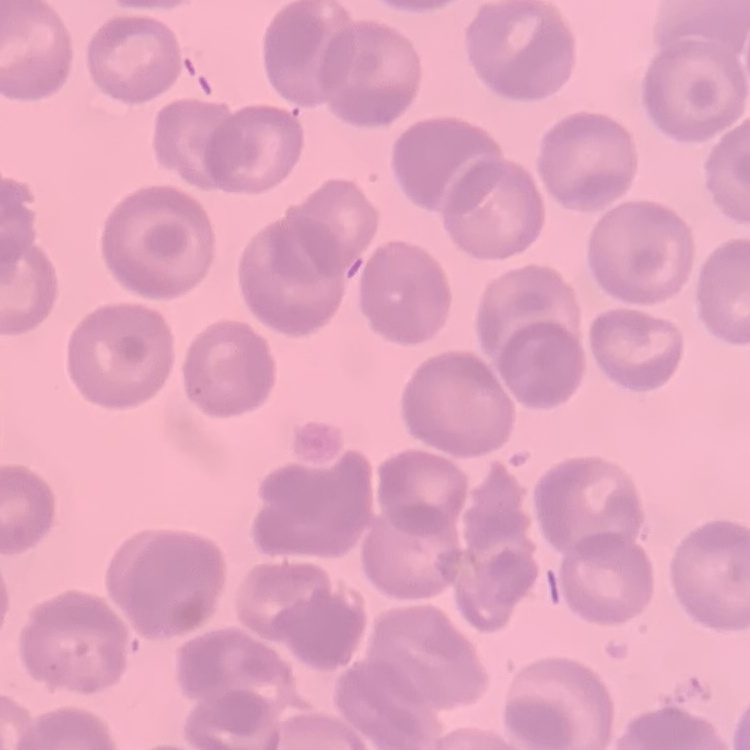

red blood cell morphology = no rouleaux formation
preparation = thin peripheral smear
stain = Field's or Giemsa
image type = one tile cut from a larger photomicrograph